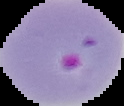

Summary:
  - Preparation: thin blood smear
  - Image size: 124×106 pixels
  - Result: Plasmodium parasites identified
  - Image type: segmented cell region on a black background